Classify this cell by malaria status.
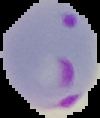

It is parasitized.

{
  "preparation": "thin blood film",
  "image_size": "100×118 pixels",
  "image_type": "segmented cell region with the area outside set to black"
}